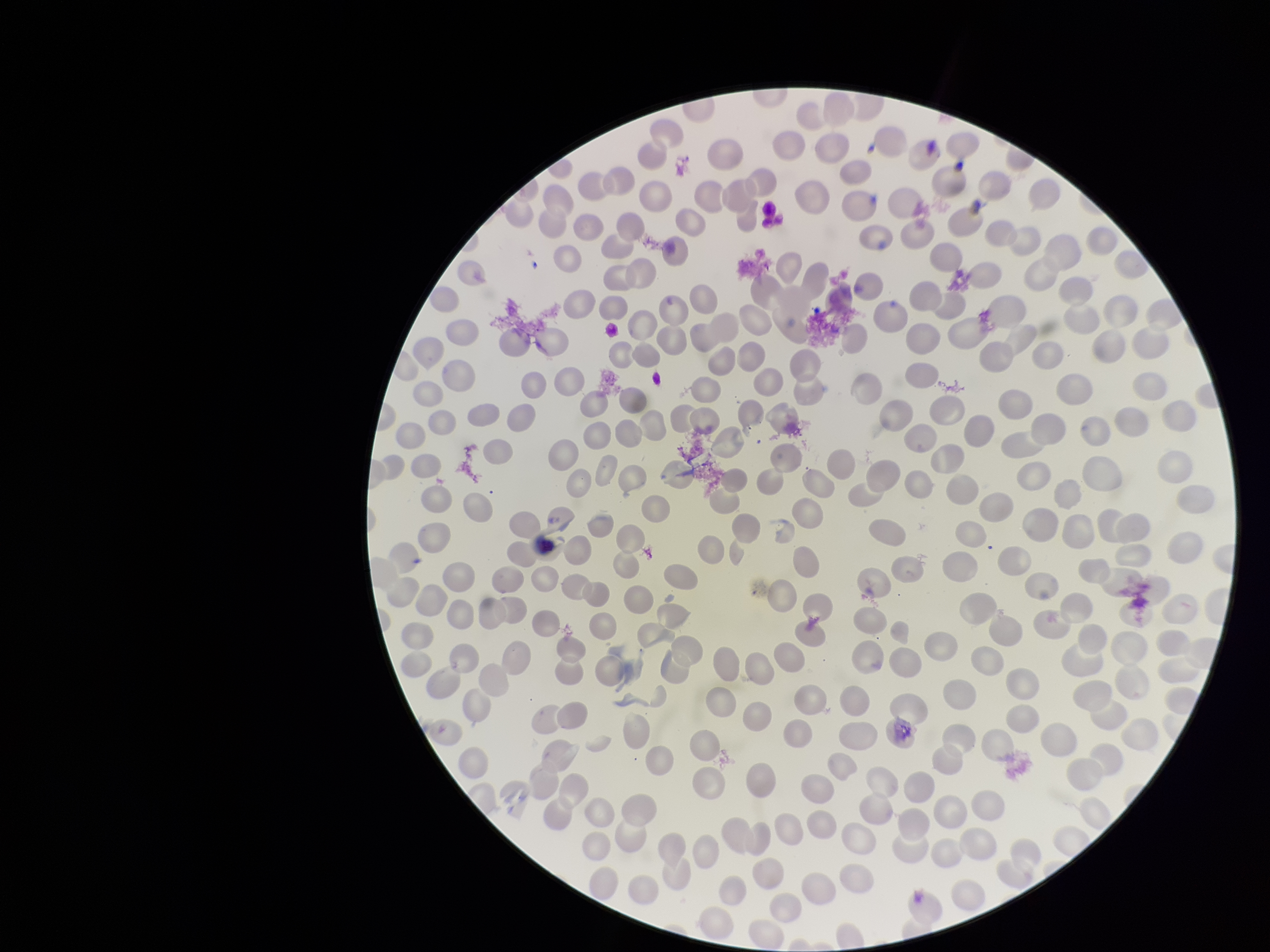
Summary:
  - Field of view: single
  - Capture: smartphone photograph through the microscope eyepiece
  - Image size: 1270×952 pixels
  - Red blood cell count: 246
  - Parasitized red blood cell count: 0
  - Parasitized red blood cells: none seen
  - Patient malaria status: negative
  - Stain: Giemsa
  - Preparation: thin blood smear